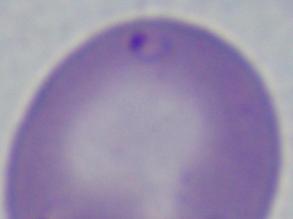
Summary:
  - Modality: micrograph
  - Identification: Babesia
  - Magnification: 1000x